Assess this cell for malaria.
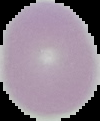

It is uninfected.

Image is 100×121 pixels. From a thin blood smear. The area outside the segmented cell region is set to black.